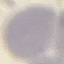
malaria status = uninfected
image type = automatically extracted cell patch, resized to 64 × 64 pixels
capture = smartphone through the microscope eyepiece
stain = Giemsa
preparation = thin blood smear